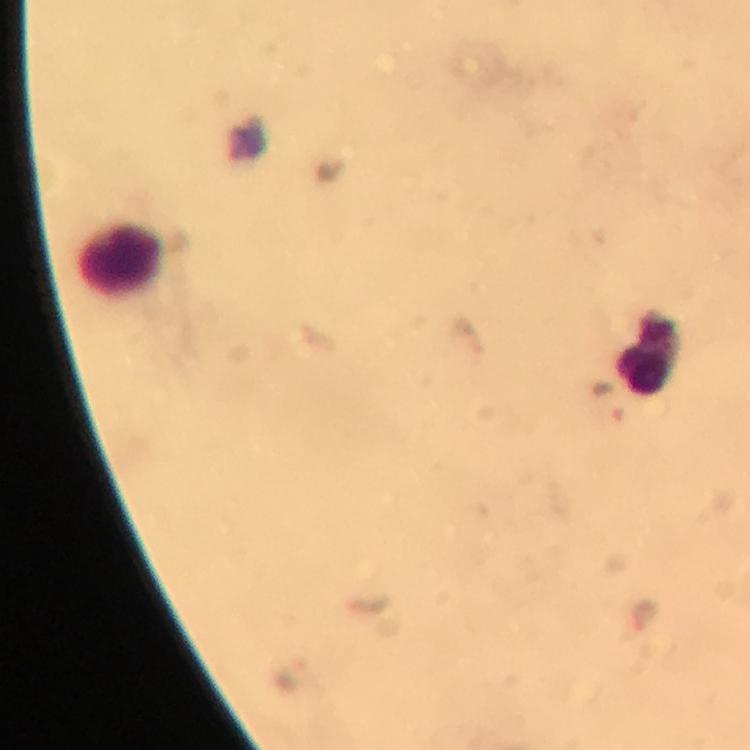

Approximate centers as (x, y) in pixels. Leukocyte locations: (123, 257), (648, 350). Malaria parasite locations: (607, 403), (644, 616), (291, 674). Immersion oil applied. 100x magnification. Image is 750×750 pixels. Giemsa stain. Photographed with a smartphone mounted on the microscope. From a malaria diagnostic workup. Thick blood smear. A crop from one field of view.